Locate every blood parasite and identify its species.
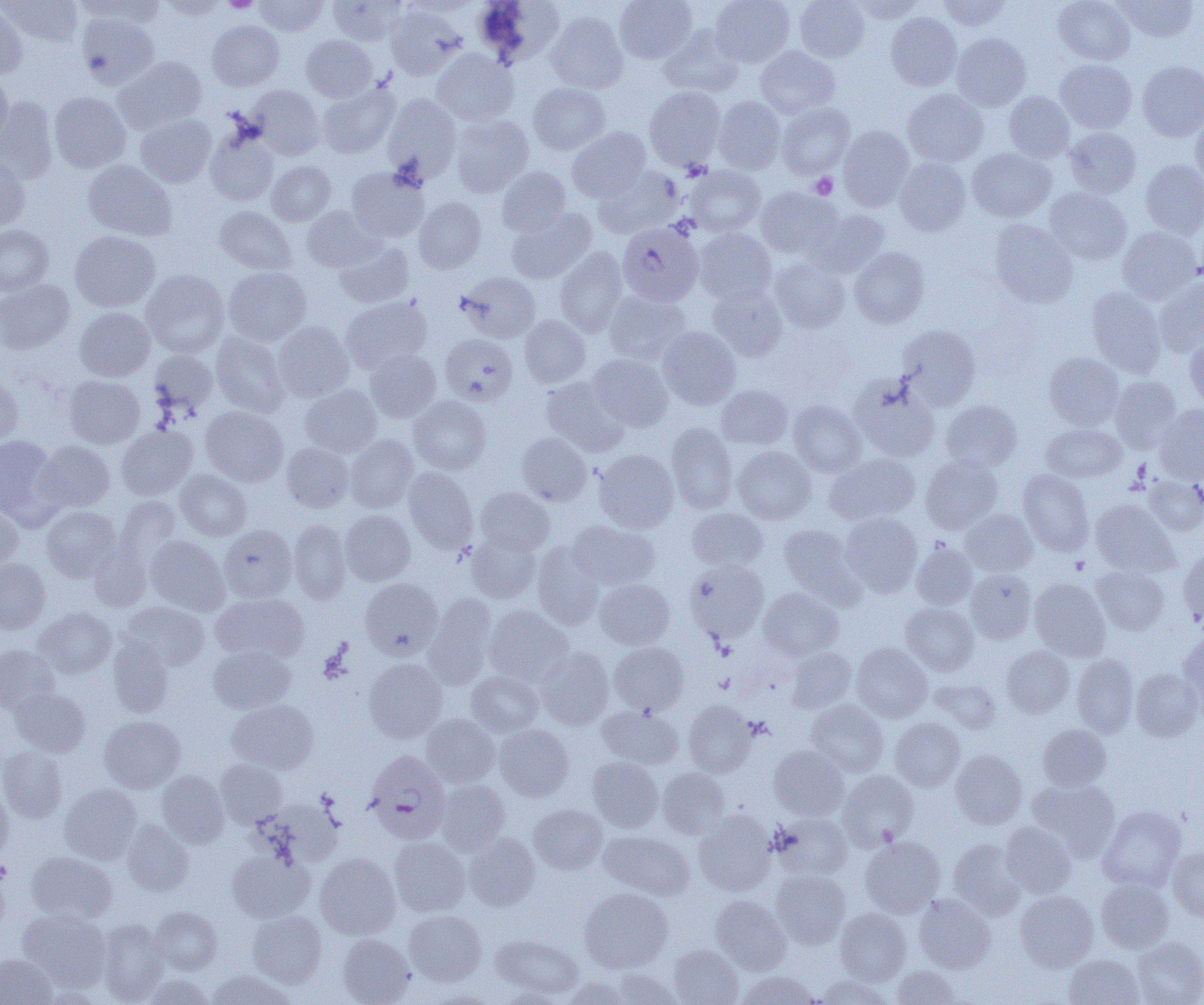
Approximate bounding boxes as [x1, y1, x2, y2] in pixels.
Plasmodium falciparum-infected red blood cells: [617, 222, 703, 306], [363, 750, 451, 845].
No Plasmodium ovale, Plasmodium malariae, Plasmodium vivax, Babesia divergens, or Trypanosoma brucei observed.

Uninfected red blood cell locations: [2, 0, 83, 47], [73, 0, 165, 29], [156, 0, 228, 20], [253, 0, 328, 36], [615, 0, 697, 64], [711, 0, 795, 67], [795, 0, 869, 62], [850, 0, 926, 23], [937, 0, 1013, 31], [1054, 0, 1134, 65], [1113, 0, 1199, 42], [327, 1, 406, 46], [477, 1, 565, 68], [0, 3, 28, 79], [385, 5, 465, 81], [545, 11, 628, 94], [76, 12, 160, 90], [886, 12, 962, 91], [207, 21, 284, 91], [659, 27, 743, 98], [952, 33, 1030, 111], [301, 35, 377, 102], [756, 46, 839, 118], [431, 49, 519, 126], [113, 56, 207, 134], [1056, 59, 1136, 132], [1137, 61, 1204, 141], [0, 75, 13, 149], [317, 82, 399, 159], [527, 83, 611, 155], [247, 84, 324, 160], [644, 87, 725, 169], [902, 89, 988, 167], [49, 91, 131, 173], [1004, 91, 1074, 162], [383, 93, 461, 182], [713, 96, 786, 175], [0, 98, 59, 183], [777, 103, 855, 179], [1191, 111, 1204, 189], [135, 114, 216, 188], [450, 114, 534, 197], [838, 126, 914, 211], [204, 127, 279, 206], [567, 127, 651, 202], [1065, 127, 1141, 198], [967, 148, 1056, 222], [0, 155, 30, 232], [894, 157, 971, 236], [82, 159, 176, 241], [1140, 159, 1204, 239], [266, 161, 335, 226], [685, 165, 765, 237], [346, 166, 429, 242], [497, 166, 571, 236], [593, 167, 682, 238], [755, 187, 841, 258], [1044, 187, 1131, 264], [413, 197, 486, 274], [302, 205, 385, 272], [214, 206, 297, 274], [506, 208, 597, 284], [807, 209, 889, 278], [988, 220, 1078, 308], [0, 225, 53, 295], [1117, 226, 1201, 304], [693, 228, 776, 304], [70, 231, 160, 312], [334, 241, 415, 309], [555, 246, 628, 337], [850, 246, 929, 328], [770, 258, 850, 333], [223, 267, 311, 346], [141, 270, 230, 358], [456, 271, 540, 343], [1153, 277, 1204, 357], [0, 279, 74, 355], [707, 284, 788, 362], [1087, 287, 1166, 376], [603, 290, 692, 365], [340, 295, 432, 373], [75, 307, 155, 381], [519, 315, 590, 387], [273, 321, 354, 402], [897, 324, 981, 410], [657, 326, 741, 410], [210, 333, 290, 417], [441, 334, 518, 405], [1185, 334, 1204, 411], [365, 349, 441, 422], [149, 350, 217, 417], [1044, 352, 1124, 430], [588, 353, 673, 431], [0, 372, 22, 448], [64, 375, 145, 449], [1109, 376, 1182, 452], [541, 377, 628, 455], [851, 377, 939, 462], [300, 384, 382, 458], [716, 385, 793, 449], [409, 395, 491, 475], [788, 400, 867, 477], [941, 400, 1021, 472], [1155, 404, 1204, 483], [201, 406, 288, 487], [666, 423, 737, 514], [1041, 424, 1126, 482], [117, 425, 197, 500], [517, 433, 591, 505], [0, 434, 60, 523], [345, 434, 418, 512], [35, 441, 115, 512], [282, 443, 354, 512], [733, 446, 816, 524], [593, 449, 678, 533], [824, 453, 920, 525], [921, 455, 1002, 534], [404, 467, 478, 553], [175, 469, 251, 541], [1018, 469, 1094, 556], [1144, 476, 1204, 535], [476, 487, 554, 556], [113, 496, 181, 572], [1090, 499, 1179, 576], [0, 503, 23, 571], [42, 506, 121, 582], [687, 507, 767, 572], [960, 509, 1037, 575], [339, 510, 415, 585], [840, 512, 922, 595], [289, 519, 350, 604], [568, 520, 659, 590], [779, 523, 862, 603], [219, 524, 297, 602], [466, 531, 541, 603], [145, 535, 229, 615], [912, 541, 978, 610], [532, 542, 605, 629], [1178, 550, 1204, 628], [0, 558, 50, 634], [685, 559, 769, 642], [1091, 566, 1170, 635], [965, 569, 1036, 643], [360, 578, 443, 659], [1029, 578, 1111, 661], [594, 579, 675, 650], [758, 587, 843, 661], [211, 592, 308, 664], [424, 593, 496, 689], [122, 601, 210, 671], [901, 603, 978, 675], [484, 605, 573, 686], [33, 608, 117, 679], [1178, 632, 1204, 716], [108, 635, 175, 717], [608, 642, 689, 715], [851, 642, 932, 723], [0, 644, 60, 713], [208, 645, 295, 713], [1002, 646, 1074, 718], [535, 647, 614, 729], [785, 647, 857, 714], [1071, 654, 1138, 737], [363, 658, 447, 743], [1131, 668, 1202, 742], [466, 671, 543, 737], [931, 678, 1001, 734], [9, 688, 91, 757], [228, 699, 319, 774], [806, 699, 888, 776], [684, 700, 756, 778], [597, 704, 683, 769], [422, 714, 499, 788], [99, 715, 186, 793], [889, 717, 964, 791], [494, 724, 574, 801], [1038, 725, 1111, 791], [769, 744, 849, 820], [0, 746, 68, 823], [950, 749, 1027, 829], [588, 757, 663, 832], [215, 759, 287, 827], [657, 768, 729, 838], [838, 769, 918, 849], [156, 770, 229, 847], [1027, 778, 1120, 860], [436, 780, 510, 855], [0, 783, 13, 862], [59, 783, 142, 864], [256, 798, 344, 867], [529, 804, 607, 874], [1098, 805, 1186, 892], [694, 810, 777, 896], [772, 812, 853, 880], [122, 819, 193, 896], [1000, 822, 1077, 897], [599, 830, 695, 900], [464, 832, 540, 911], [389, 837, 470, 916], [860, 837, 946, 917], [948, 838, 1026, 919], [1168, 847, 1204, 922], [226, 850, 313, 922], [26, 851, 117, 924], [315, 853, 401, 940], [0, 869, 10, 941], [771, 870, 851, 948], [1096, 878, 1174, 953], [579, 887, 673, 973], [1015, 890, 1099, 972], [913, 893, 995, 973], [711, 895, 791, 974], [150, 906, 222, 974], [835, 908, 911, 985], [17, 909, 112, 992], [247, 909, 327, 988], [404, 910, 486, 985], [97, 919, 169, 1003], [338, 934, 415, 1005], [490, 934, 583, 998], [1132, 937, 1204, 1005], [669, 944, 743, 1004], [0, 953, 57, 1005], [1063, 954, 1144, 1004], [891, 965, 961, 1005], [606, 968, 683, 1004], [207, 970, 296, 1005], [736, 970, 822, 1004], [814, 973, 894, 1005], [140, 974, 216, 1004], [560, 976, 633, 1004]. Platelet locations: [222, 0, 258, 13], [810, 173, 837, 199], [1070, 557, 1089, 574], [714, 673, 735, 693], [0, 860, 12, 883]. Slide-level diagnosis: Plasmodium falciparum. 1000x magnification. Light microscopy. Thin blood film. One field of a larger specimen. Image is 1204×1005 pixels.